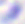
Micrograph. 400x magnification. Toxoplasma gondii is seen.